Classify this cell by malaria status.
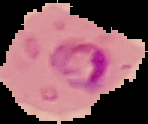

It is parasitized.

The area outside the segmented cell region is set to black. Image is 148×124 pixels. From a thin blood smear.